Give the extent of all uninfected red blood cells.
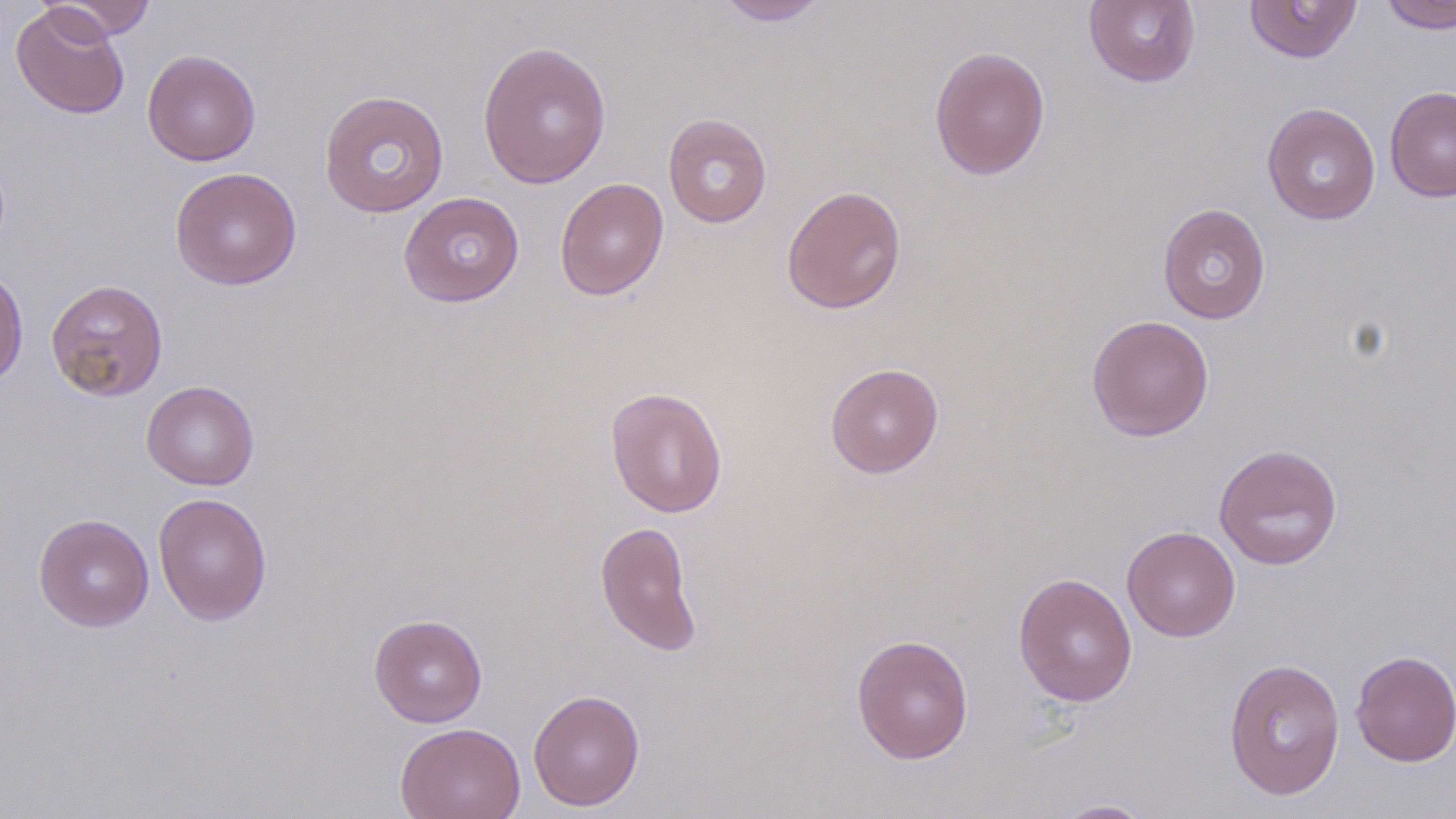
Approximate bounding boxes as named x1/y1/x2/y2 corners in pixels.
Uninfected red blood cells: (x1=43, y1=0, x2=156, y2=40), (x1=715, y1=0, x2=830, y2=26), (x1=1083, y1=0, x2=1201, y2=88), (x1=1244, y1=0, x2=1363, y2=63), (x1=1379, y1=0, x2=1456, y2=34), (x1=10, y1=4, x2=130, y2=119), (x1=476, y1=40, x2=612, y2=189), (x1=929, y1=45, x2=1050, y2=180), (x1=142, y1=48, x2=261, y2=166), (x1=1385, y1=85, x2=1456, y2=202), (x1=318, y1=89, x2=450, y2=219), (x1=1262, y1=102, x2=1380, y2=225), (x1=662, y1=114, x2=772, y2=228), (x1=170, y1=166, x2=302, y2=290), (x1=555, y1=177, x2=669, y2=300), (x1=781, y1=184, x2=907, y2=314), (x1=398, y1=191, x2=525, y2=307), (x1=1157, y1=202, x2=1271, y2=324), (x1=0, y1=268, x2=28, y2=390), (x1=45, y1=278, x2=168, y2=402), (x1=1086, y1=314, x2=1214, y2=441), (x1=825, y1=362, x2=944, y2=478), (x1=141, y1=380, x2=259, y2=490), (x1=605, y1=387, x2=727, y2=518), (x1=1214, y1=443, x2=1343, y2=570), (x1=153, y1=492, x2=272, y2=625), (x1=34, y1=513, x2=154, y2=631), (x1=594, y1=520, x2=704, y2=657), (x1=1122, y1=525, x2=1240, y2=641), (x1=1012, y1=572, x2=1138, y2=707), (x1=369, y1=613, x2=488, y2=727), (x1=851, y1=633, x2=974, y2=765), (x1=1350, y1=649, x2=1455, y2=767), (x1=1223, y1=657, x2=1346, y2=801), (x1=528, y1=688, x2=645, y2=811), (x1=394, y1=722, x2=526, y2=819), (x1=1052, y1=799, x2=1157, y2=818).

Slide-level diagnosis: negative for blood parasites. Single field of view. Optical microscopy. Captured at 1000x magnification. May-Grünwald-Giemsa stain. Thin blood film. Image is 1456×819 pixels.